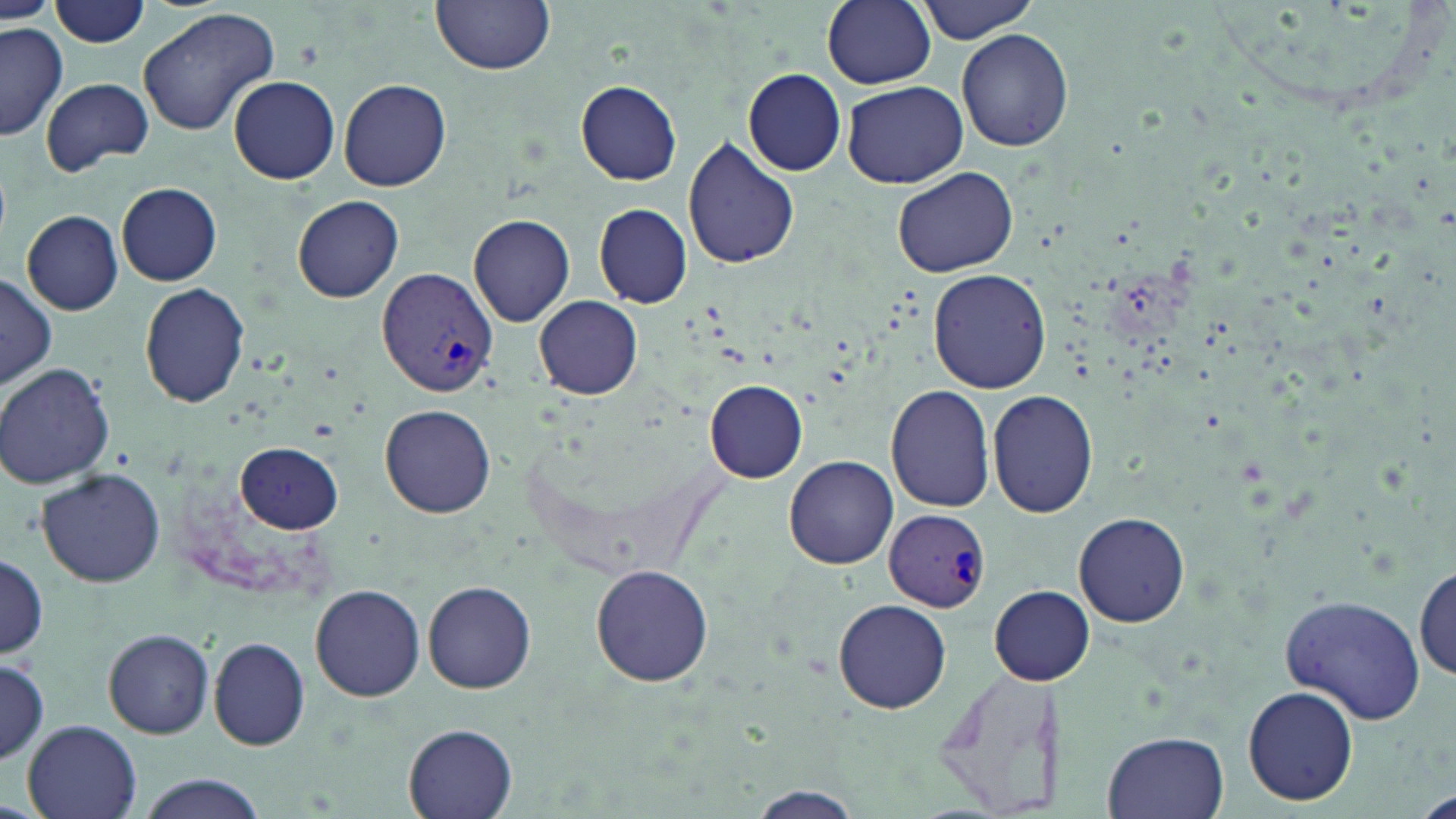

Summary:
  - Coordinate format: approximate bounding boxes as [x1, y1, x2, y2] in pixels
  - Plasmodium vivax-infected red blood cell locations: [377, 267, 496, 398], [886, 509, 992, 612]
  - Uninfected red blood cell locations: [433, 0, 556, 74], [822, 0, 935, 89], [916, 0, 1040, 42], [50, 1, 151, 47], [0, 3, 56, 25], [138, 5, 281, 137], [0, 20, 67, 141], [956, 27, 1074, 151], [742, 69, 845, 176], [229, 75, 340, 184], [41, 76, 154, 176], [339, 78, 451, 191], [577, 80, 683, 185], [841, 80, 969, 187], [681, 138, 798, 269], [892, 167, 1018, 277], [116, 182, 222, 285], [293, 196, 404, 303], [594, 204, 692, 307], [23, 210, 124, 314], [469, 214, 575, 326], [928, 268, 1052, 393], [0, 273, 57, 389], [139, 283, 249, 406], [535, 295, 644, 399], [0, 362, 116, 489], [705, 380, 807, 483], [887, 384, 995, 512], [988, 390, 1097, 517], [380, 403, 495, 517], [235, 442, 343, 532], [784, 456, 897, 570], [37, 469, 165, 587], [1073, 511, 1190, 627], [0, 554, 47, 658], [1415, 563, 1455, 681], [590, 564, 714, 686], [423, 580, 536, 693], [311, 584, 426, 701], [989, 585, 1094, 684], [1281, 594, 1428, 723], [833, 599, 952, 714], [103, 628, 214, 738], [208, 638, 312, 750], [0, 657, 48, 765], [929, 665, 1071, 816], [1242, 684, 1359, 808], [21, 719, 144, 819], [403, 721, 519, 819], [1102, 731, 1231, 818], [132, 774, 270, 819], [747, 787, 865, 819]
  - Slide-level diagnosis: Plasmodium vivax
  - Field of view: one of a larger specimen
  - Modality: optical microscopy
  - Stain: May-Grünwald-Giemsa
  - Preparation: thin blood film
  - Image size: 1456×819 pixels
  - Magnification: 1000x